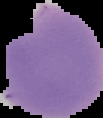

Summary:
  - Image size: 103×118 pixels
  - Image type: segmented cell region on a black background
  - Preparation: thin blood smear
  - Malaria status: parasitized